Assess this cell for malaria.
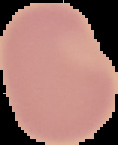
Uninfected.

Image is 118×145 pixels. From a thin blood film. Segmented cell region on a black background.